Give the extent of all Plasmodium malariae-infected red blood cells.
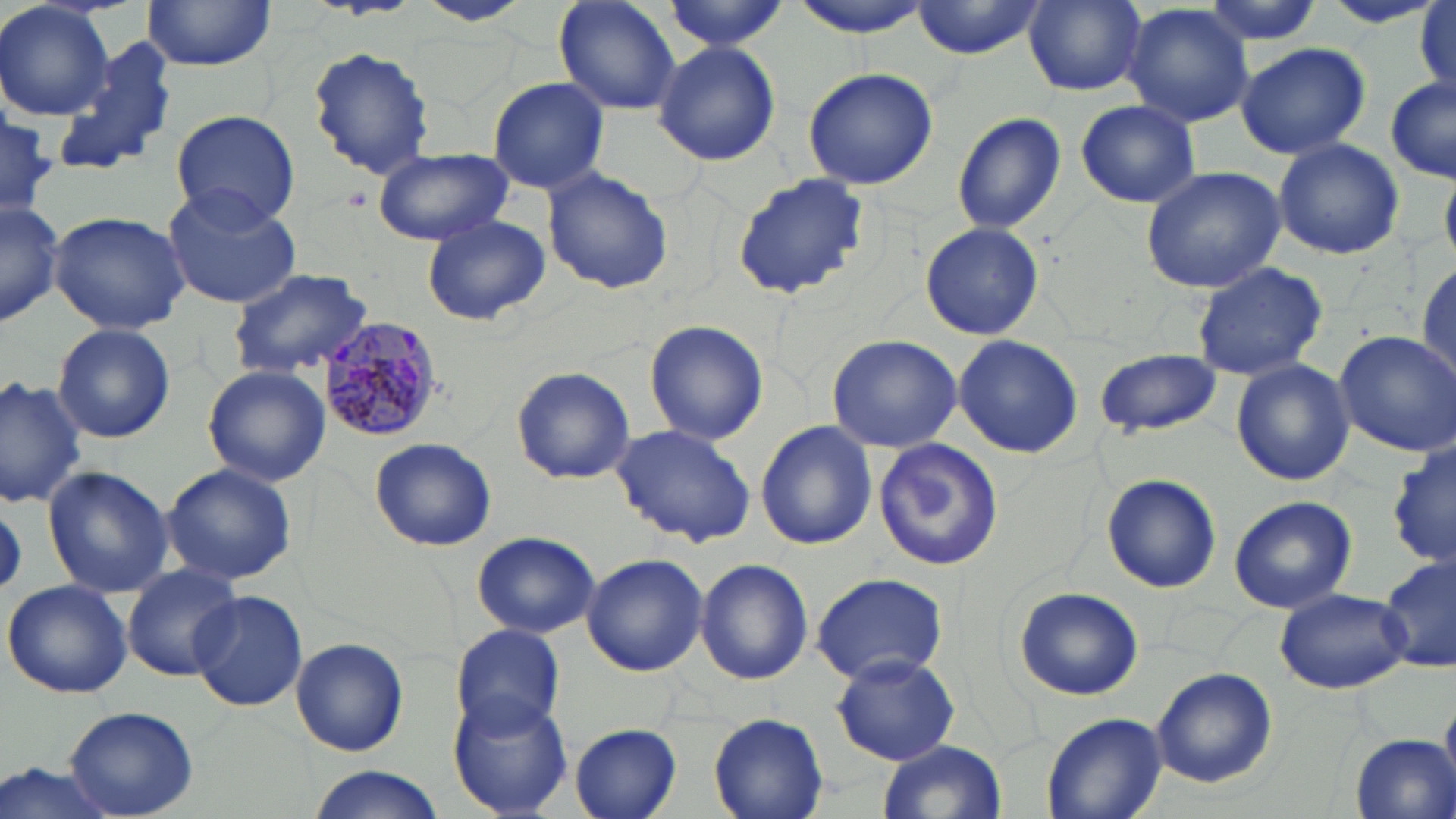

Approximate bounding boxes as named x1/y1/x2/y2 corners in pixels.
Plasmodium malariae-infected red blood cells: (x1=315, y1=315, x2=442, y2=442).

{
  "slide_level_diagnosis": "Plasmodium malariae",
  "preparation": "thin blood film",
  "magnification": "1000x",
  "field_of_view": "one of a larger specimen",
  "image_size": "1456×819 pixels",
  "modality": "optical microscopy",
  "uninfected_red_blood_cell_locations": "approximate bounding boxes as named x1/y1/x2/y2 corners in pixels: (x1=416, y1=0, x2=535, y2=28), (x1=553, y1=0, x2=682, y2=115), (x1=786, y1=0, x2=935, y2=36), (x1=911, y1=0, x2=1050, y2=59), (x1=1197, y1=0, x2=1325, y2=46), (x1=1316, y1=0, x2=1444, y2=29), (x1=0, y1=1, x2=116, y2=120), (x1=1023, y1=1, x2=1147, y2=96), (x1=140, y1=2, x2=275, y2=73), (x1=660, y1=2, x2=789, y2=52), (x1=1415, y1=4, x2=1454, y2=92), (x1=1124, y1=5, x2=1255, y2=129), (x1=45, y1=41, x2=182, y2=182), (x1=653, y1=41, x2=781, y2=167), (x1=1234, y1=41, x2=1372, y2=159), (x1=307, y1=45, x2=436, y2=179), (x1=801, y1=65, x2=938, y2=191), (x1=486, y1=76, x2=611, y2=194), (x1=1385, y1=76, x2=1456, y2=184), (x1=1074, y1=100, x2=1200, y2=208), (x1=170, y1=110, x2=299, y2=228), (x1=952, y1=113, x2=1066, y2=234), (x1=0, y1=117, x2=58, y2=213), (x1=1272, y1=137, x2=1404, y2=260), (x1=372, y1=149, x2=514, y2=247), (x1=543, y1=166, x2=673, y2=296), (x1=1140, y1=166, x2=1285, y2=293), (x1=732, y1=172, x2=871, y2=300), (x1=160, y1=186, x2=301, y2=309), (x1=1, y1=198, x2=66, y2=327), (x1=49, y1=208, x2=191, y2=336), (x1=420, y1=215, x2=551, y2=328), (x1=921, y1=220, x2=1044, y2=341), (x1=1190, y1=261, x2=1327, y2=381), (x1=1416, y1=261, x2=1454, y2=379), (x1=226, y1=267, x2=374, y2=379), (x1=643, y1=320, x2=768, y2=446), (x1=52, y1=322, x2=177, y2=443), (x1=1333, y1=332, x2=1456, y2=457), (x1=826, y1=334, x2=962, y2=453), (x1=953, y1=335, x2=1084, y2=460), (x1=1095, y1=347, x2=1222, y2=437), (x1=1231, y1=359, x2=1355, y2=487), (x1=202, y1=363, x2=330, y2=486), (x1=512, y1=366, x2=633, y2=484), (x1=0, y1=374, x2=90, y2=509), (x1=754, y1=421, x2=878, y2=550), (x1=609, y1=424, x2=757, y2=546), (x1=370, y1=436, x2=497, y2=551), (x1=871, y1=437, x2=1004, y2=574), (x1=161, y1=463, x2=297, y2=585), (x1=42, y1=465, x2=174, y2=597), (x1=1101, y1=472, x2=1220, y2=593), (x1=1229, y1=497, x2=1356, y2=612), (x1=472, y1=532, x2=600, y2=639), (x1=1379, y1=552, x2=1455, y2=674), (x1=582, y1=553, x2=708, y2=677), (x1=694, y1=558, x2=813, y2=686), (x1=122, y1=563, x2=243, y2=681), (x1=809, y1=571, x2=951, y2=685), (x1=3, y1=578, x2=133, y2=698), (x1=1013, y1=585, x2=1144, y2=701), (x1=1272, y1=587, x2=1411, y2=694), (x1=188, y1=590, x2=306, y2=712), (x1=450, y1=625, x2=567, y2=735), (x1=291, y1=637, x2=409, y2=758), (x1=832, y1=652, x2=962, y2=766), (x1=1150, y1=667, x2=1277, y2=789), (x1=448, y1=693, x2=573, y2=816), (x1=66, y1=707, x2=199, y2=817), (x1=1041, y1=711, x2=1166, y2=819), (x1=708, y1=713, x2=828, y2=819), (x1=568, y1=724, x2=683, y2=819), (x1=1350, y1=734, x2=1454, y2=818), (x1=878, y1=739, x2=1008, y2=819), (x1=0, y1=762, x2=122, y2=819), (x1=306, y1=767, x2=444, y2=819)",
  "stain": "May-Grünwald-Giemsa"
}